Identify the parasite.
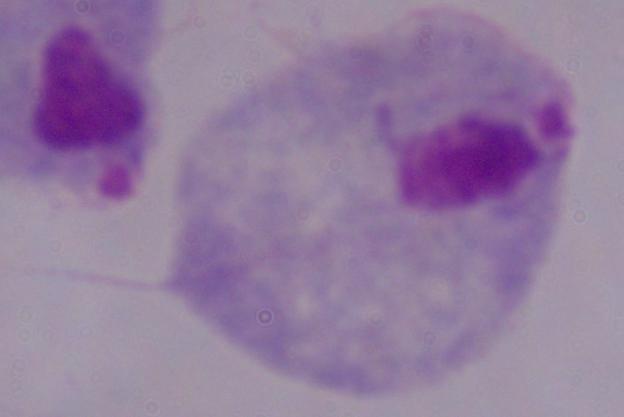

A trichomonad.

Summary:
  - Modality: micrograph
  - Magnification: 1000x